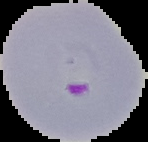
Summary:
  - Preparation: thin blood smear
  - Image type: segmented cell region with the area outside set to black
  - Image size: 148×142 pixels
  - Malaria status: parasitized